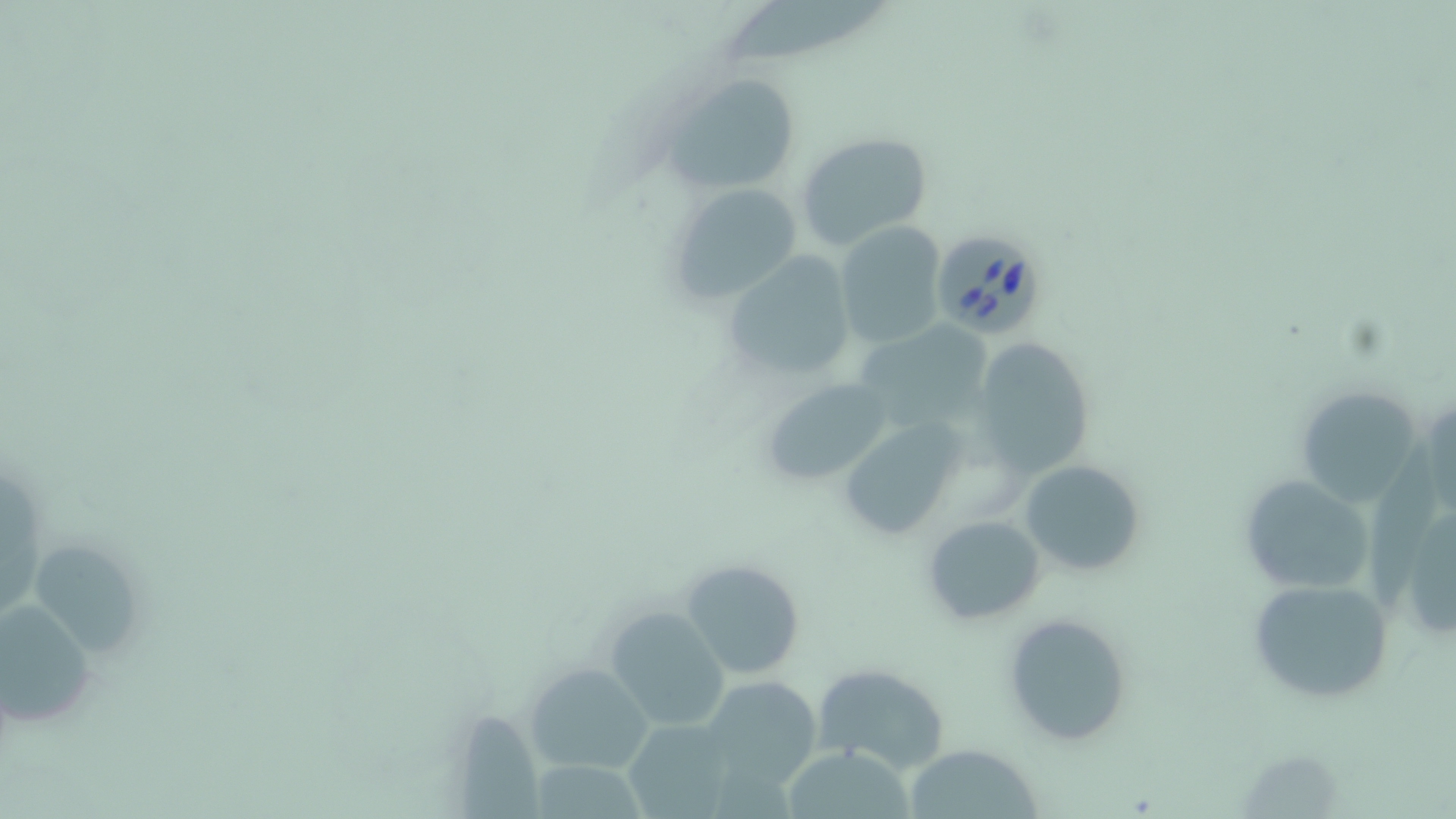

Summary:
  - Coordinate format: approximate bounding boxes as (x1,y1)-(x2,y2) corner pairs in pixels
  - Uninfected red blood cell locations: (727,0)-(896,65), (660,70)-(804,194), (796,132)-(933,252), (668,181)-(804,304), (834,222)-(946,347), (721,252)-(855,383), (860,322)-(1008,428), (972,337)-(1096,478), (757,377)-(895,487), (1293,384)-(1429,510), (839,419)-(964,538), (1018,458)-(1145,579), (1237,473)-(1374,597), (1380,489)-(1456,646), (920,514)-(1047,625), (35,545)-(140,665), (681,558)-(808,681), (1247,575)-(1396,703), (0,598)-(99,727), (607,606)-(731,730), (1004,612)-(1134,746), (524,663)-(656,773), (811,664)-(952,777), (699,675)-(823,792), (453,710)-(543,819), (622,718)-(738,817), (904,742)-(1041,818), (781,747)-(916,817), (535,753)-(658,819)
  - Babesia divergens-infected red blood cell locations: (928,228)-(1047,338)
  - Slide-level diagnosis: Babesia divergens
  - Image size: 1456×819 pixels
  - Modality: light microscopy
  - Stain: May-Grünwald-Giemsa
  - Preparation: thin blood film
  - Magnification: 1000x
  - Field of view: one of a larger specimen